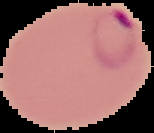
Summary:
  - Preparation: thin blood smear
  - Image size: 154×133 pixels
  - Malaria status: parasitized
  - Image type: segmented cell region on a black background